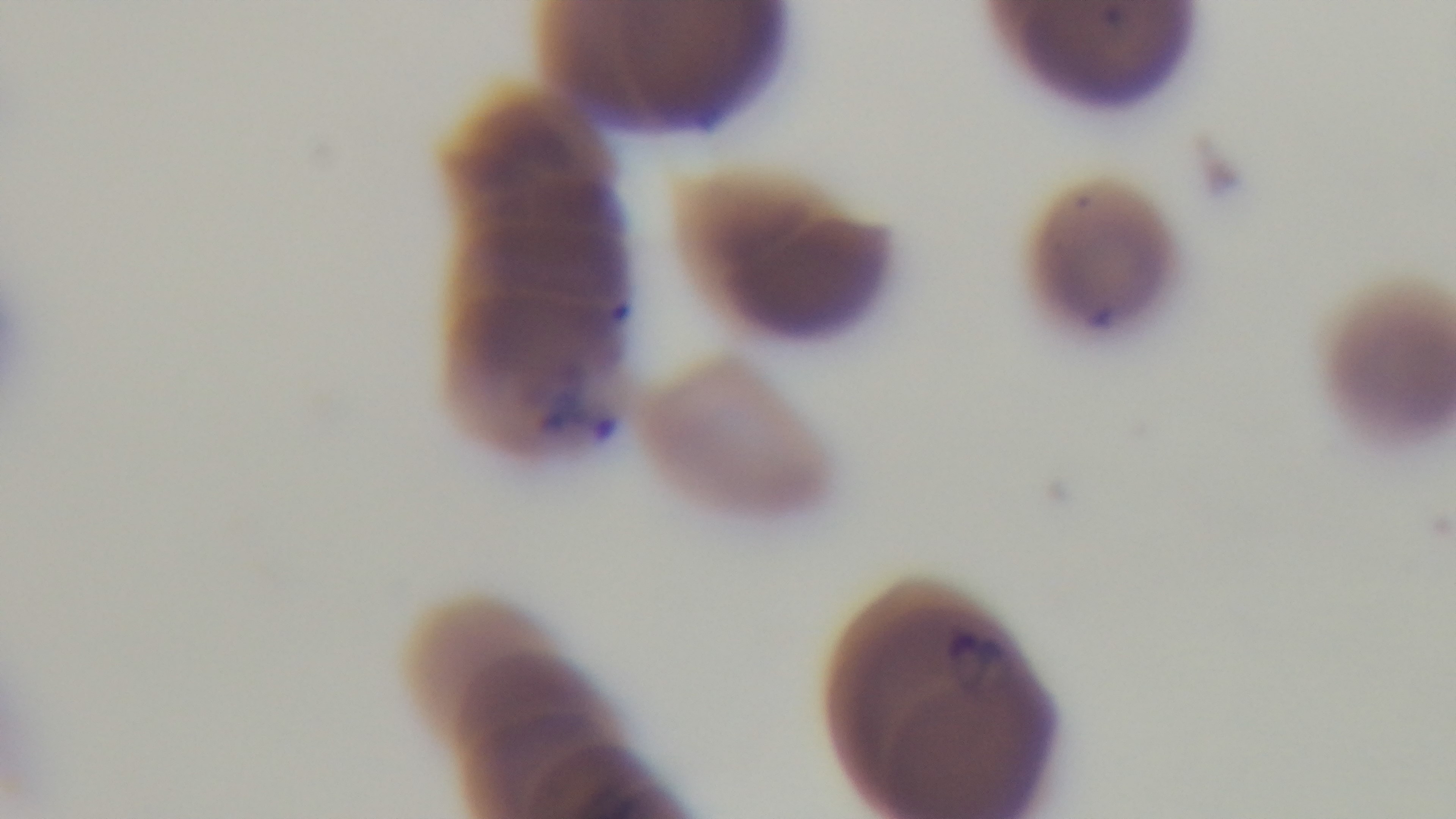 100x oil-immersion objective. Giemsa-stained. One field from the slide. Photomicrograph. Preparation: thin blood film. Malaria status: positive. Captured with a mounted 4K digital camera.